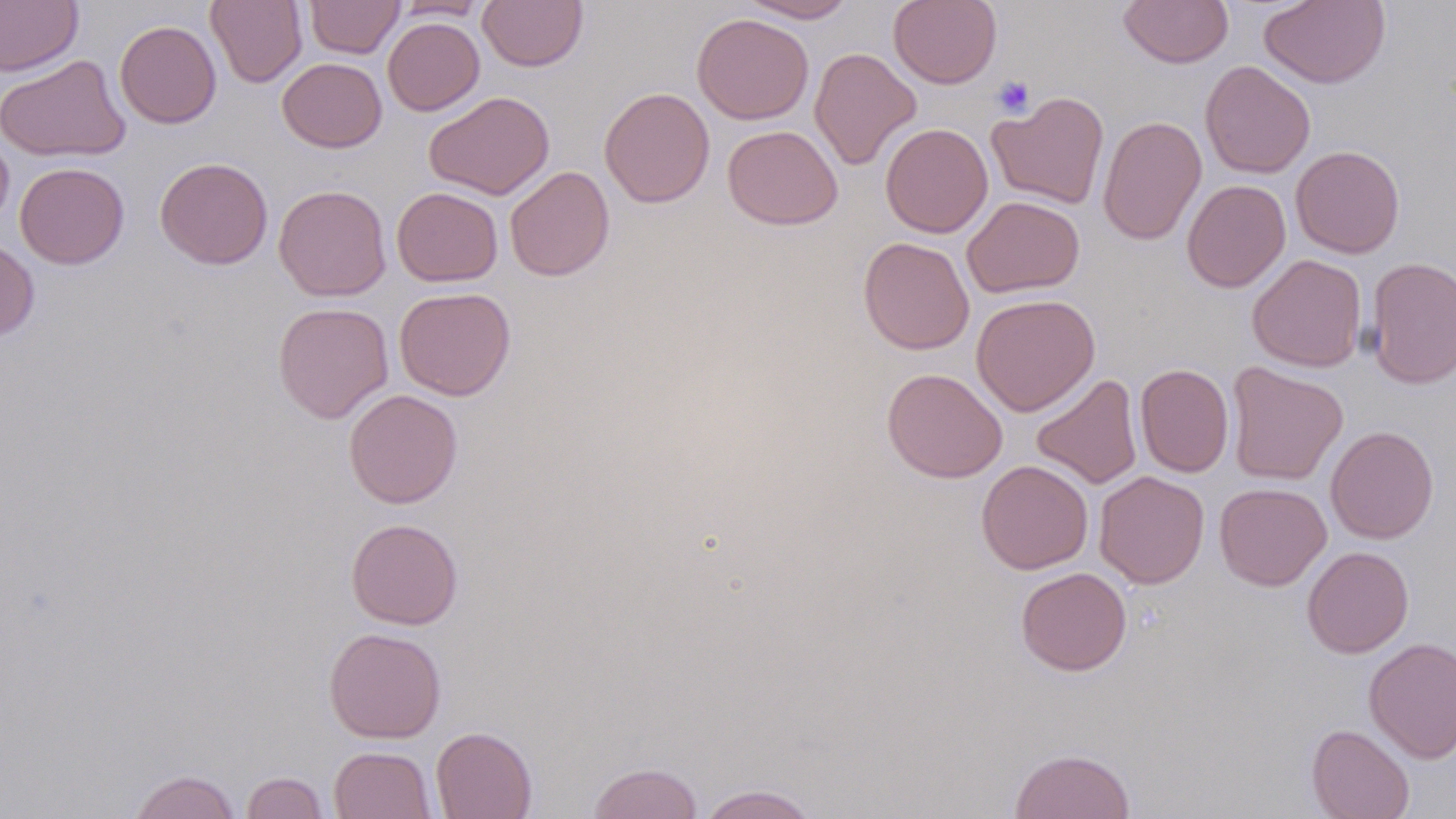

slide_level_diagnosis: negative for blood parasites
image_size: 1456×819 pixels
preparation: thin blood film
uninfected_red_blood_cell_locations: 'approximate bounding boxes as [x1, y1, x2, y2] in pixels: [0, 0, 83, 76], [206, 0, 307, 88], [304, 0, 405, 59], [477, 0, 588, 72], [740, 0, 858, 23], [888, 0, 1002, 89], [1118, 0, 1233, 68], [1258, 0, 1391, 89], [393, 1, 489, 21], [691, 12, 814, 125], [383, 17, 485, 116], [115, 20, 222, 129], [809, 48, 922, 171], [0, 54, 131, 162], [277, 58, 387, 153], [1199, 60, 1315, 178], [599, 86, 714, 208], [988, 90, 1109, 209], [424, 91, 555, 200], [1097, 115, 1207, 246], [880, 123, 993, 238], [722, 125, 843, 230], [0, 132, 14, 231], [1290, 145, 1406, 258], [155, 157, 273, 270], [15, 162, 129, 269], [505, 166, 615, 281], [1181, 179, 1290, 292], [274, 184, 391, 301], [391, 187, 503, 286], [962, 196, 1084, 298], [859, 236, 975, 355], [0, 238, 39, 342], [1247, 254, 1367, 372], [1365, 256, 1456, 389], [394, 286, 516, 401], [971, 293, 1100, 416], [272, 302, 394, 423], [1226, 362, 1348, 486], [1135, 363, 1234, 478], [882, 368, 1007, 483], [1031, 374, 1142, 489], [343, 389, 463, 508], [1325, 425, 1439, 544], [976, 460, 1094, 574], [1094, 470, 1210, 588], [1214, 482, 1332, 590], [346, 518, 463, 629], [1301, 545, 1414, 658], [1015, 566, 1132, 676], [323, 627, 446, 743], [1364, 637, 1456, 762], [1306, 723, 1415, 819], [430, 726, 538, 819], [329, 746, 437, 819], [1009, 747, 1136, 819], [587, 761, 704, 819], [128, 769, 241, 819], [241, 771, 329, 818], [697, 784, 819, 819]'
magnification: 1000x
modality: light microscopy
field_of_view: one of a larger specimen
stain: May-Grünwald-Giemsa
platelet_locations: 'approximate bounding boxes as [x1, y1, x2, y2] in pixels: [992, 75, 1035, 118]'